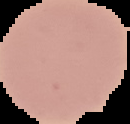
{
  "malaria_status": "uninfected",
  "image_size": "130×124 pixels",
  "image_type": "cell region segmented out of the field of view; surrounding area masked to black",
  "preparation": "thin blood smear"
}